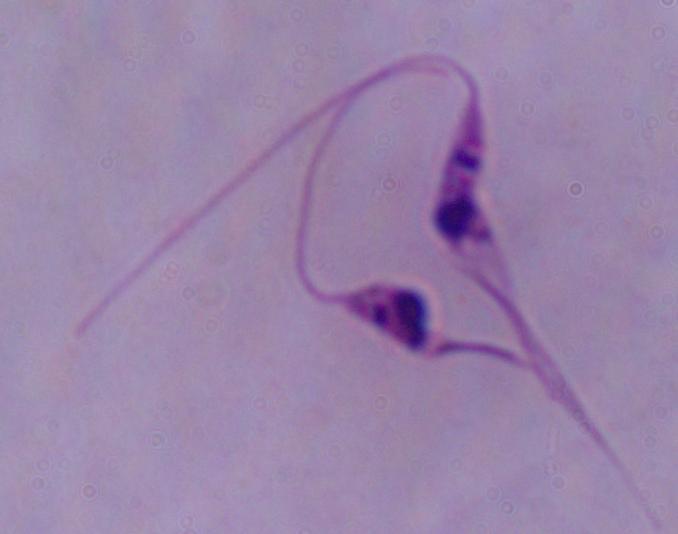

Summary:
  - Identification: Leishmania
  - Magnification: 1000x
  - Modality: photomicrograph